Assess the morphology of the red blood cells.
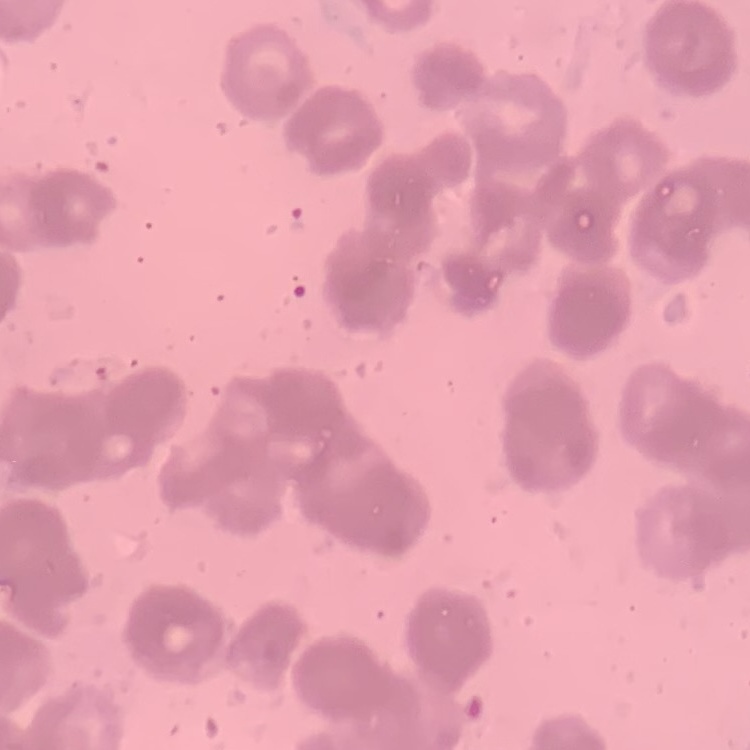
They show rouleaux formation.

{
  "stain": "Field's or Giemsa",
  "image_type": "square crop of a larger photomicrograph",
  "preparation": "thin blood film"
}